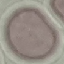
Malaria status: uninfected. Giemsa stain. Cell patch, automatically extracted from a larger field of view and resized to 64 × 64 pixels. Thin smear of blood. Acquired by smartphone through the microscope eyepiece.